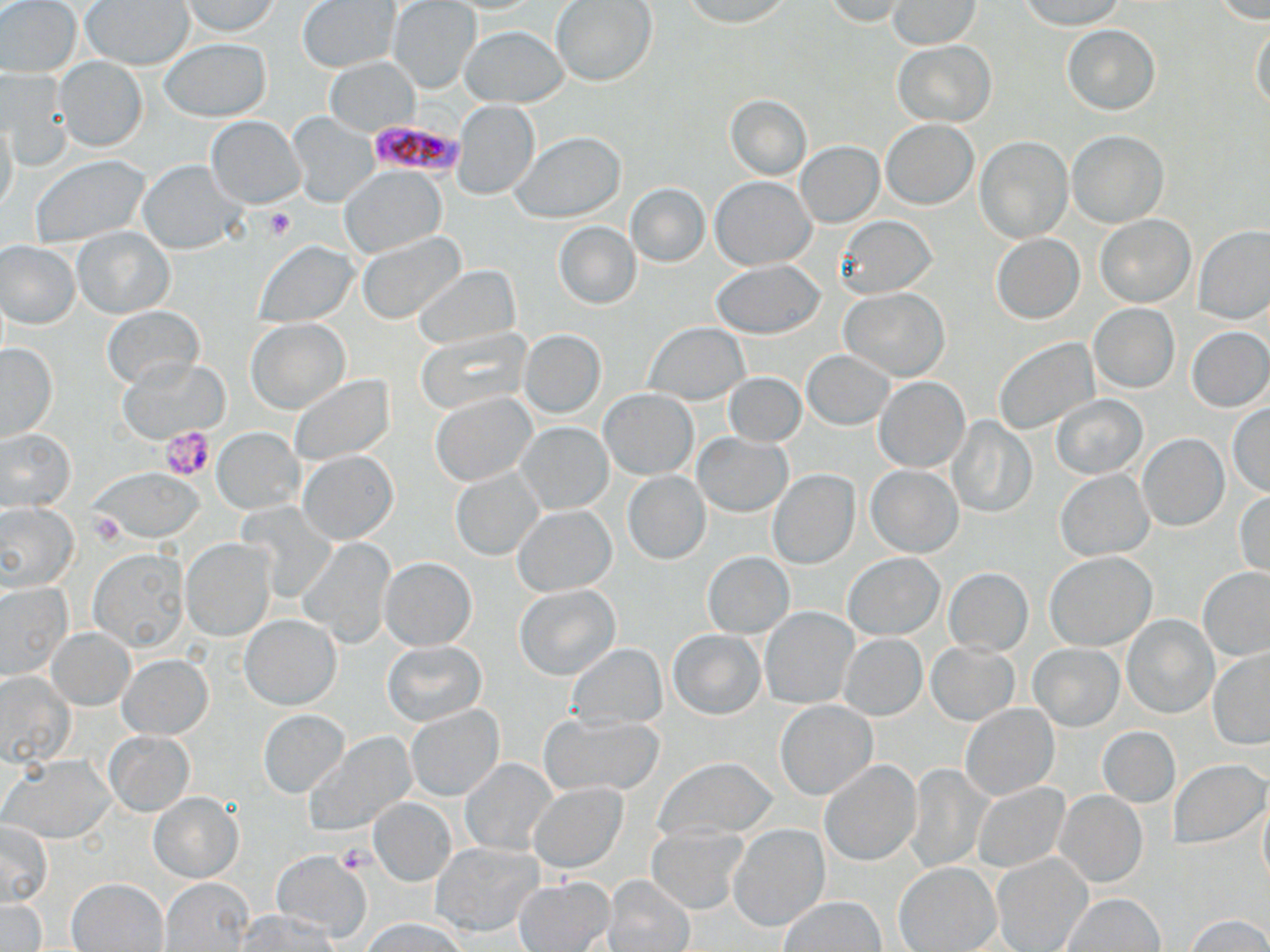

slide-level diagnosis = Plasmodium falciparum
platelet locations = approximate bounding boxes as (x1, y1, x2, y2) in pixels: (263, 207, 295, 241), (161, 425, 216, 481), (336, 843, 371, 874)
modality = optical microscopy
Plasmodium falciparum-infected red blood cell locations = approximate bounding boxes as (x1, y1, x2, y2) in pixels: (368, 119, 462, 178)
magnification = 1000x
field of view = single
preparation = thin blood film
stain = May-Grünwald-Giemsa
image size = 1270×952 pixels
uninfected red blood cell locations = approximate bounding boxes as (x1, y1, x2, y2) in pixels: (1, 0, 81, 76), (181, 0, 281, 37), (678, 0, 795, 27), (821, 0, 911, 26), (889, 0, 981, 49), (1015, 0, 1127, 30), (1209, 0, 1270, 22), (82, 1, 194, 69), (297, 1, 399, 73), (388, 1, 481, 92), (550, 1, 657, 87), (1249, 23, 1270, 114), (1061, 24, 1161, 115), (459, 25, 569, 107), (159, 38, 271, 122), (893, 40, 997, 127), (326, 57, 418, 134), (55, 58, 147, 152), (2, 70, 74, 169), (725, 94, 811, 180), (452, 99, 540, 199), (288, 113, 376, 205), (206, 114, 305, 208), (880, 118, 978, 209), (0, 120, 18, 216), (1067, 131, 1168, 227), (511, 132, 626, 223), (974, 135, 1072, 242), (795, 142, 883, 226), (30, 154, 150, 246), (139, 160, 242, 254), (341, 167, 444, 254), (711, 176, 814, 269), (625, 183, 709, 267), (835, 214, 936, 297), (1095, 214, 1195, 308), (552, 221, 641, 310), (1193, 224, 1270, 324), (72, 228, 175, 319), (356, 230, 464, 324), (990, 233, 1084, 324), (254, 241, 357, 327), (1, 242, 80, 328), (711, 260, 827, 338), (411, 264, 519, 351), (840, 288, 950, 380), (1088, 302, 1180, 393), (102, 305, 204, 389), (247, 318, 350, 412), (644, 322, 750, 405), (1186, 326, 1269, 412), (415, 328, 528, 414), (518, 330, 606, 418), (993, 336, 1099, 436), (0, 343, 58, 442), (802, 350, 895, 430), (118, 356, 226, 441), (724, 373, 805, 446), (288, 374, 396, 463), (876, 376, 970, 472), (600, 389, 697, 478), (432, 392, 536, 485), (1051, 394, 1148, 480), (1227, 404, 1270, 496), (948, 417, 1036, 519), (517, 421, 612, 512), (213, 427, 302, 513), (1, 428, 74, 510), (1136, 433, 1228, 532), (693, 434, 792, 516), (298, 450, 398, 543), (866, 465, 963, 557), (451, 468, 544, 560), (90, 469, 208, 542), (769, 469, 859, 569), (1055, 469, 1154, 560), (622, 471, 711, 565), (1235, 492, 1270, 577), (0, 501, 79, 591), (513, 504, 616, 595), (180, 538, 275, 641), (297, 538, 396, 647), (89, 548, 189, 650), (703, 551, 794, 638), (1045, 551, 1157, 649), (844, 552, 944, 639), (379, 557, 476, 650), (943, 567, 1033, 656), (1199, 567, 1270, 661), (0, 582, 71, 679), (513, 584, 620, 679), (761, 607, 859, 708), (241, 614, 341, 709), (1121, 614, 1218, 718), (48, 627, 134, 709), (668, 628, 766, 719), (838, 634, 926, 721), (927, 640, 1019, 725), (382, 641, 487, 726), (568, 643, 667, 729), (1029, 644, 1124, 731), (1207, 649, 1270, 750), (119, 656, 212, 739), (0, 671, 75, 767), (774, 700, 877, 800), (960, 704, 1058, 800), (406, 705, 503, 801), (259, 708, 351, 798), (540, 714, 664, 797), (1098, 726, 1180, 807), (105, 730, 193, 816), (308, 732, 415, 836), (7, 755, 113, 841), (656, 756, 777, 842), (460, 757, 557, 855), (1170, 759, 1267, 848), (818, 760, 920, 865), (904, 765, 991, 871), (974, 782, 1068, 872), (528, 783, 627, 872), (1056, 790, 1147, 887), (149, 793, 242, 882), (1259, 796, 1270, 888), (370, 799, 456, 884), (1, 821, 53, 905), (730, 824, 828, 931), (647, 825, 747, 914), (432, 842, 543, 935), (272, 851, 371, 939), (992, 851, 1092, 952), (894, 861, 1000, 951), (604, 873, 695, 952), (514, 876, 615, 950), (163, 877, 254, 952), (68, 878, 168, 951), (1062, 893, 1165, 951), (779, 897, 885, 951), (0, 899, 45, 950), (240, 910, 343, 951), (1185, 914, 1270, 951), (365, 918, 465, 952)